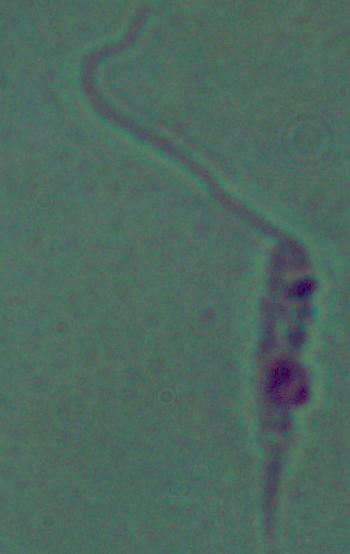
1000x magnification. Micrograph. A Leishmania parasite is seen.